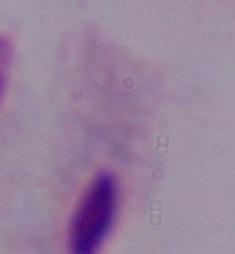
magnification: 1000x
identification: trichomonad
modality: micrograph